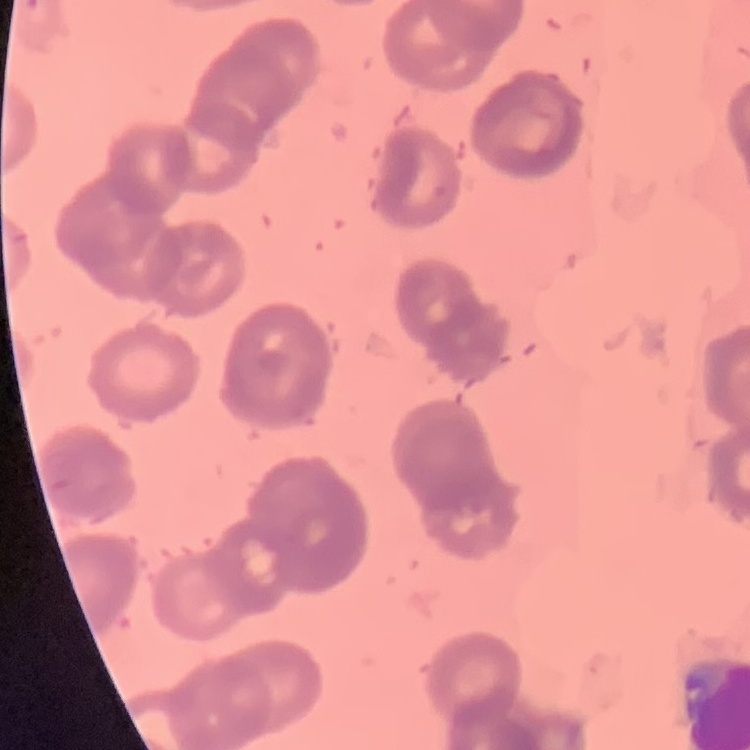 The erythrocytes exhibit rouleaux formation. Stained with either Field's or Giemsa. One tile cut from a larger photomicrograph. Thin peripheral smear.